Report the malaria status of this cell.
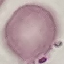
Uninfected.

capture: smartphone through the microscope eyepiece
preparation: thin smear
stain: Giemsa
image_type: cell patch, automatically extracted from a larger field of view and resized to 64 × 64 pixels